Assess this cell for malaria.
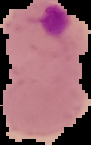
It is parasitized.

From a thin blood smear. Image is 91×145 pixels. Segmented cell region on a black background.